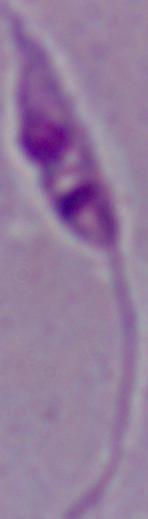
Summary:
  - Identification: Leishmania
  - Modality: photomicrograph
  - Magnification: 1000x